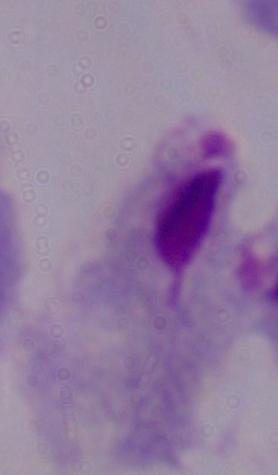

Summary:
  - Identification: trichomonad
  - Modality: micrograph
  - Magnification: 1000x